Outline platelets.
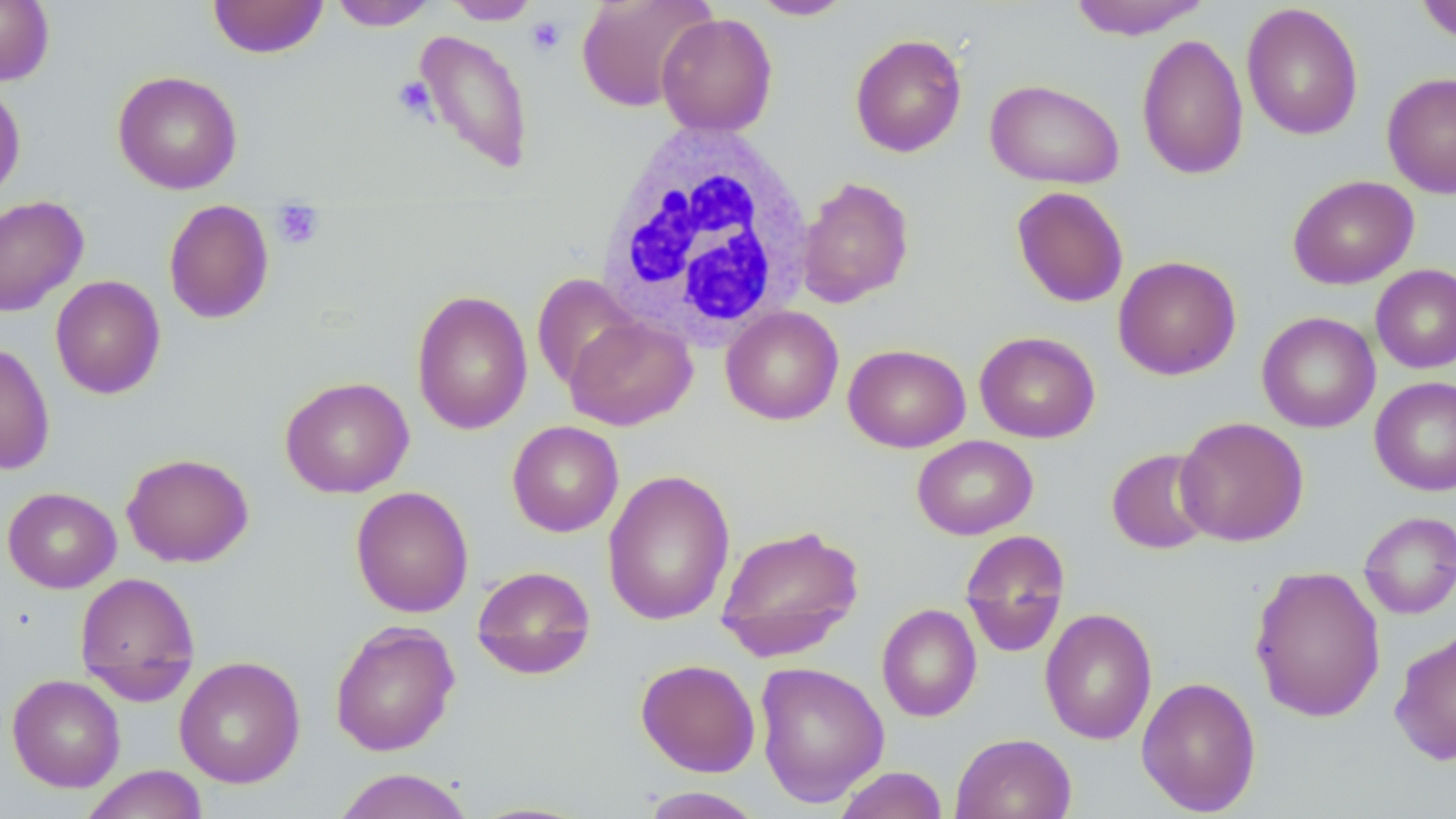

Approximate bounding boxes as (x1, y1, x2, y2) in pixels.
Platelets: (526, 15, 566, 56), (392, 76, 436, 121), (271, 199, 325, 251).

slide_level_diagnosis: negative for blood parasites
image_size: 1456×819 pixels
preparation: thin blood smear
modality: light microscopy
field_of_view: one of a larger specimen
white_blood_cell_locations: 'approximate bounding boxes as (x1, y1, x2, y2) in pixels: (594, 122, 817, 348)'
stain: May-Grünwald-Giemsa
magnification: 1000x
uninfected_red_blood_cell_locations: 'approximate bounding boxes as (x1, y1, x2, y2) in pixels: (0, 0, 55, 85), (207, 0, 329, 58), (575, 0, 715, 112), (749, 0, 857, 20), (1067, 0, 1211, 40), (1414, 0, 1456, 43), (328, 1, 438, 31), (443, 1, 542, 25), (1241, 3, 1364, 141), (656, 13, 778, 136), (413, 29, 534, 175), (849, 32, 967, 158), (1137, 33, 1249, 180), (112, 70, 243, 195), (1381, 71, 1456, 198), (984, 78, 1124, 189), (0, 82, 26, 203), (1287, 175, 1419, 289), (796, 176, 914, 307), (1011, 186, 1129, 308), (0, 195, 89, 316), (163, 199, 274, 324), (1113, 255, 1242, 380), (1371, 264, 1456, 373), (531, 274, 641, 390), (50, 275, 166, 399), (411, 289, 533, 435), (720, 306, 844, 425), (1257, 311, 1380, 433), (564, 315, 698, 431), (974, 331, 1100, 443), (0, 342, 55, 475), (843, 344, 970, 452), (279, 376, 414, 498), (1369, 376, 1456, 496), (1174, 416, 1309, 546), (507, 420, 624, 537), (912, 435, 1038, 540), (1106, 448, 1217, 555), (121, 452, 254, 568), (602, 468, 736, 626), (3, 486, 121, 593), (351, 486, 474, 617), (1358, 510, 1456, 619), (715, 523, 866, 660), (959, 530, 1070, 656), (1249, 564, 1386, 723), (470, 565, 596, 680), (74, 572, 200, 698), (876, 604, 982, 722), (1039, 607, 1158, 745), (330, 620, 460, 757), (1389, 628, 1456, 766), (174, 656, 305, 789), (635, 658, 761, 777), (754, 661, 890, 807), (7, 674, 125, 792), (1136, 675, 1261, 815), (950, 733, 1076, 819), (80, 765, 208, 819), (832, 766, 949, 819), (330, 768, 476, 819), (637, 786, 769, 818)'